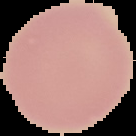

Summary:
  - Preparation: thin blood film
  - Image size: 136×136 pixels
  - Image type: segmented cell region with the area outside set to black
  - Malaria status: uninfected